Report the malaria status of this cell.
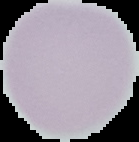

It is uninfected.

Image is 139×142 pixels. The area outside the segmented cell region is set to black. From a thin blood film.